Identify the cell.
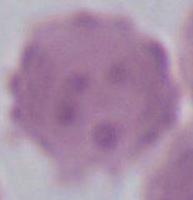
An erythrocyte.

Photomicrograph. Captured at 1000x magnification.